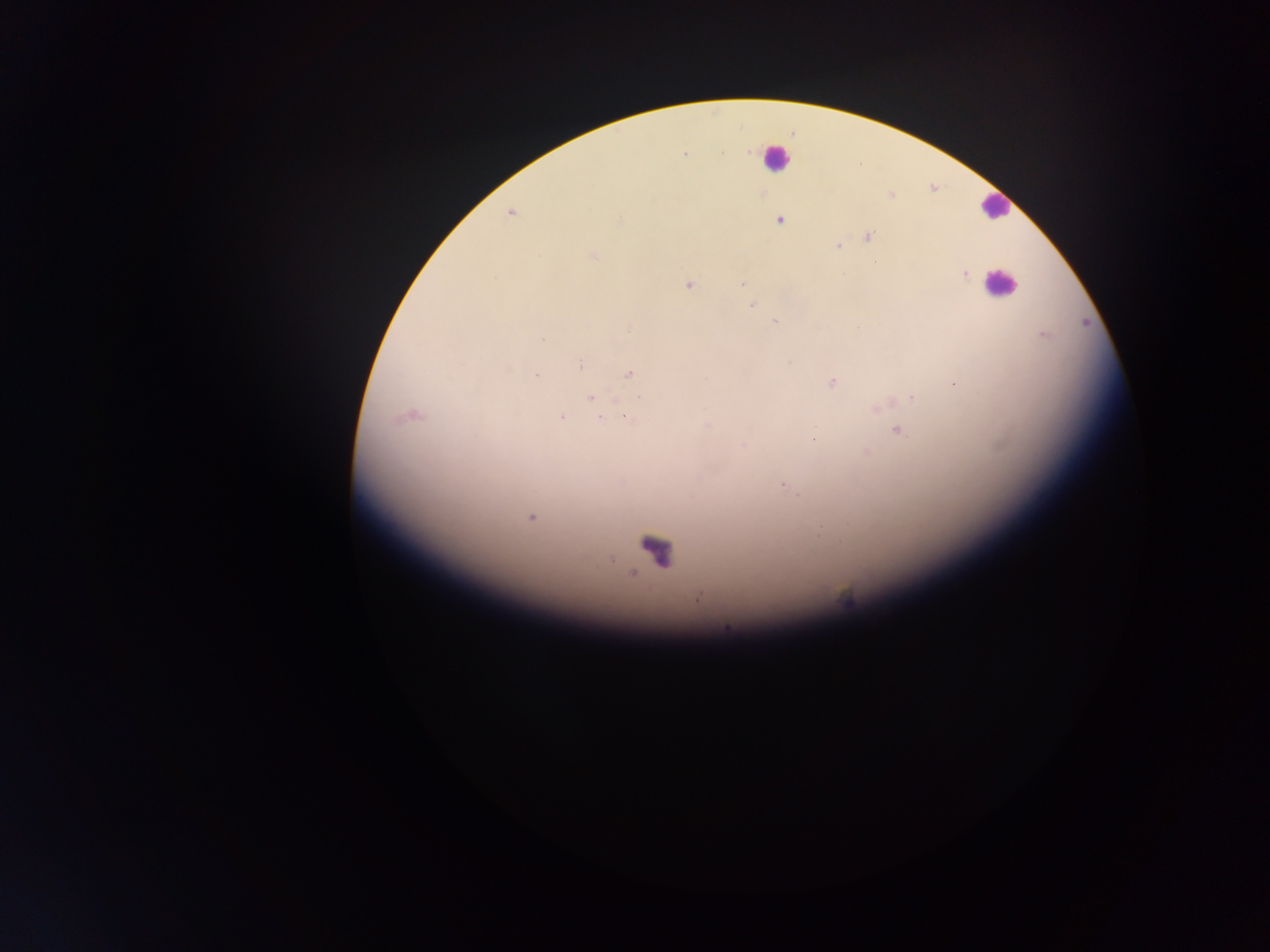
Approximate centers as x y in pixels.
Summary:
  - Plasmodium parasite locations: 722 152; 749 152; 685 154; 891 195; 510 213; 779 220; 620 221; 869 238; 837 246; 592 255; 965 274; 741 284; 688 285; 752 305; 775 322; 1043 335; 542 340; 789 363; 580 365; 629 373; 537 375; 832 382; 955 383; 590 398; 912 398; 412 415; 561 417; 628 418; 601 419; 898 431; 814 439; 743 445; 867 453; 783 485; 531 517; 698 599; 847 600; 726 627
  - Leukocyte locations: 775 157; 995 206; 1000 282; 655 549
  - Capture: mobile-phone photograph through a microscope
  - Preparation: thick blood film
  - Field of view: single
  - Country: Ghana
  - Image size: 1270×952 pixels